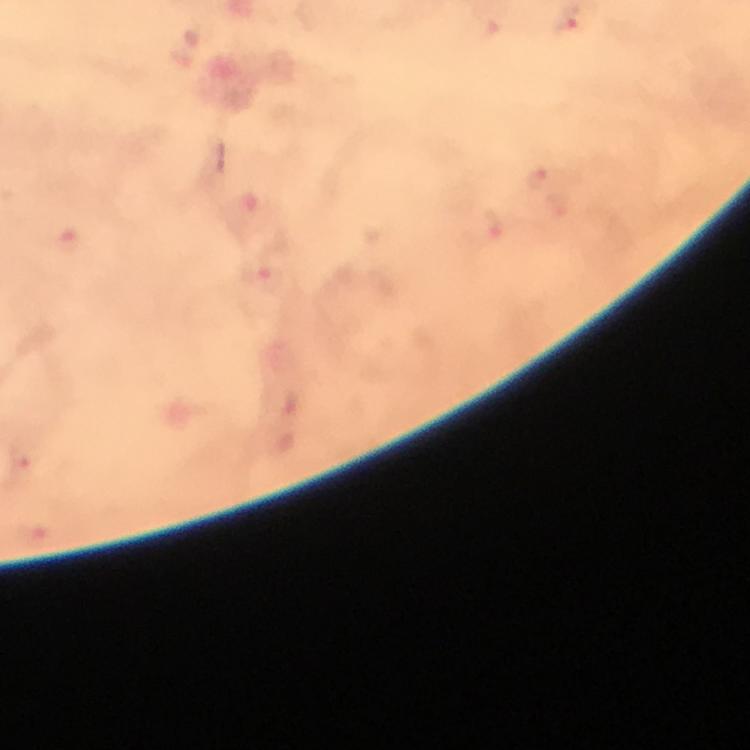
immersion oil = applied
malaria parasite locations = approximate centers as (x, y) in pixels: (535, 177), (264, 276), (18, 462)
image size = 750×750 pixels
preparation = thick smear
stain = Giemsa
magnification = 100x
context = from a diagnostic examination for malaria
cropped from = a single field of view
capture = smartphone mounted on the microscope